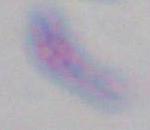

1000x magnification. Micrograph. Toxoplasma gondii is shown.